Assess the morphology of the red blood cells.
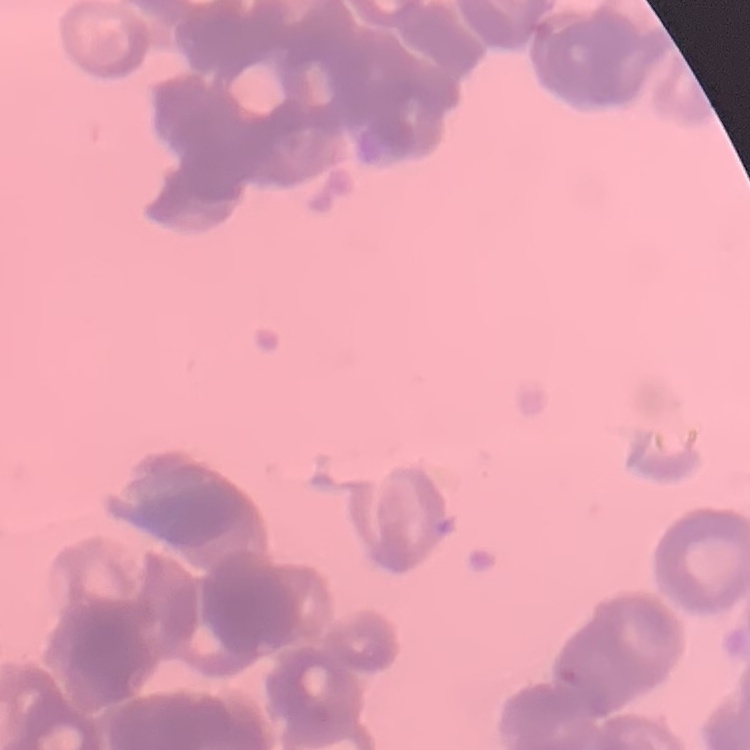
Rouleaux formation.

Summary:
  - Stain: Field's or Giemsa
  - Image type: one tile cut from a larger photomicrograph
  - Preparation: thin peripheral smear